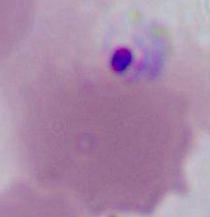

Summary:
  - Identification: Plasmodium
  - Modality: micrograph
  - Magnification: 400x or 1000x